Evaluate for malaria.
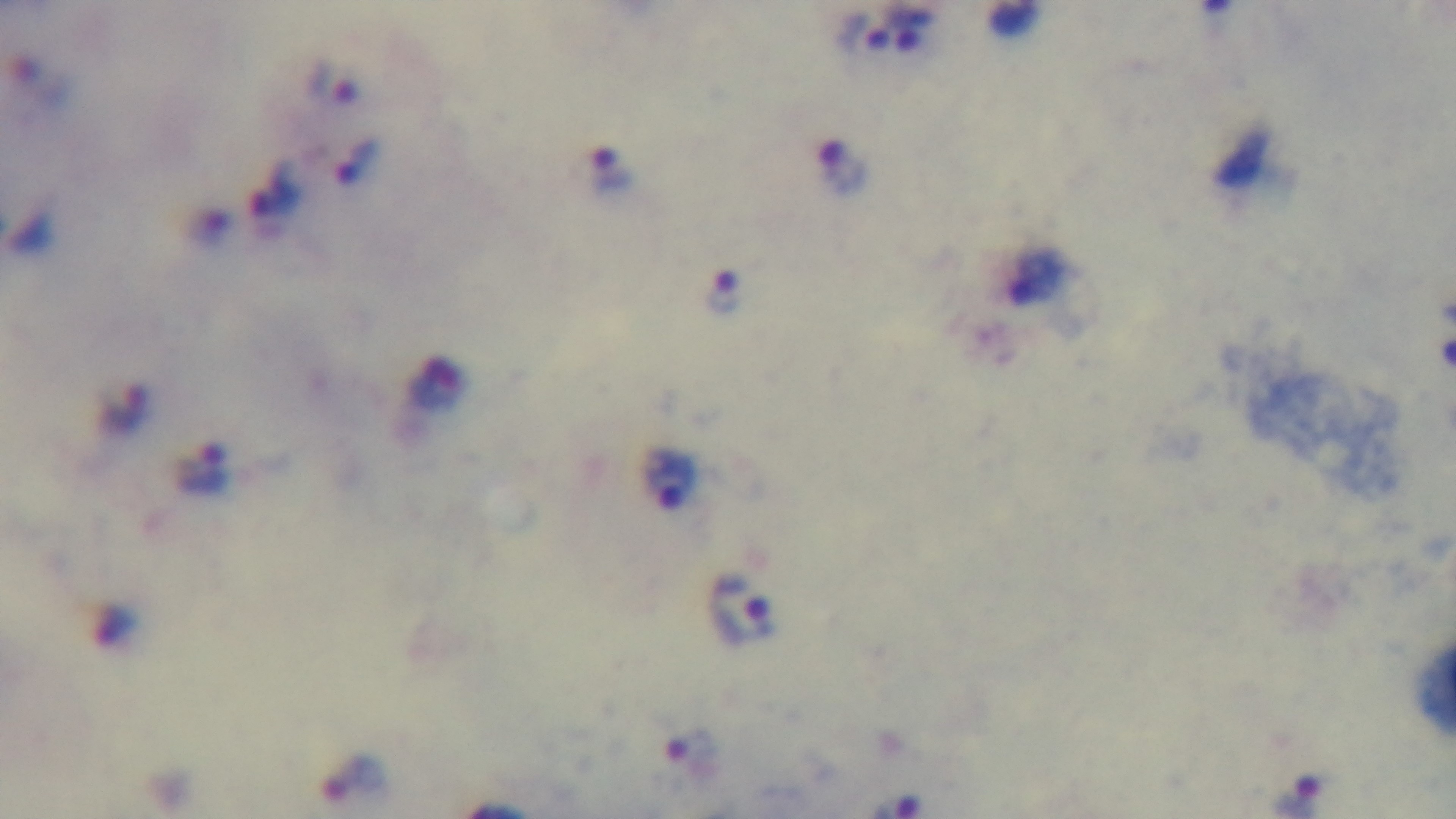
It is infected.

Giemsa stain. One field from the slide. Light microscopy. Oil-immersion objective, 100x. Preparation: thick. Mounted 4K digital camera.